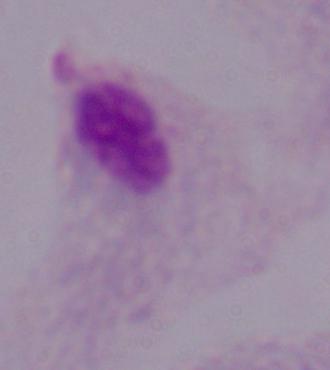 1000x magnification. Micrograph. A trichomonad is seen.